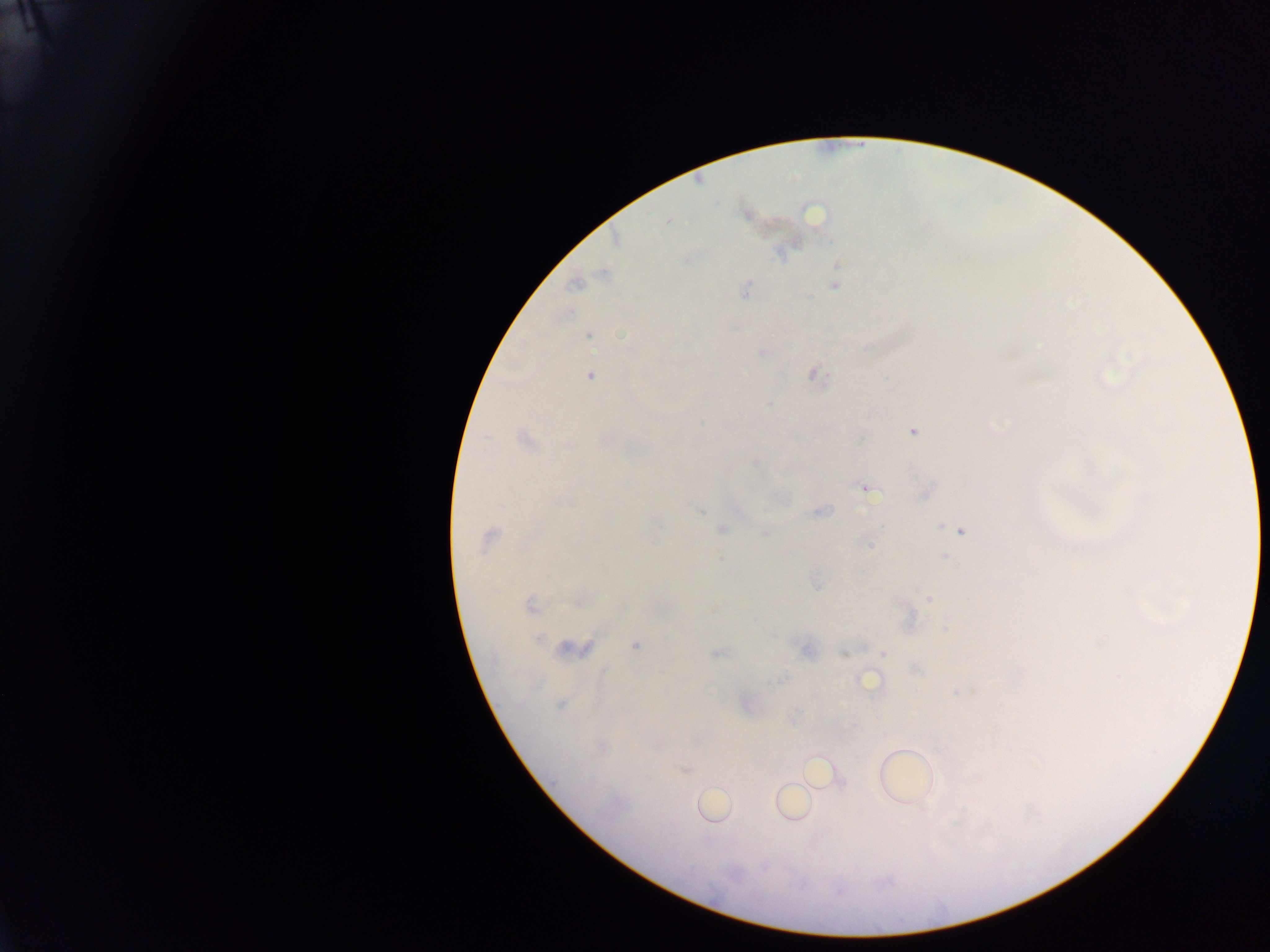

Approximate centers as (x, y) in pixels.
Summary:
  - Plasmodium parasite locations: (668, 221), (575, 284), (834, 286), (745, 289), (589, 335), (762, 352), (816, 375), (590, 376), (769, 404), (913, 431), (607, 438), (525, 439), (570, 445), (756, 461), (866, 488), (823, 510), (699, 511), (941, 525), (722, 529), (961, 531), (765, 533), (488, 536), (867, 544), (946, 557), (929, 598), (531, 607), (909, 620), (946, 627), (1104, 636), (538, 638), (635, 645), (573, 649), (806, 650), (718, 652), (843, 653), (884, 653), (917, 670), (1119, 676), (782, 679), (869, 682), (560, 705), (747, 705), (684, 770)
  - Country: Ghana
  - Field of view: single
  - Capture: mobile-phone photograph through a microscope
  - Preparation: thick blood smear
  - Image size: 1270×952 pixels